Describe the morphology of the erythrocytes.
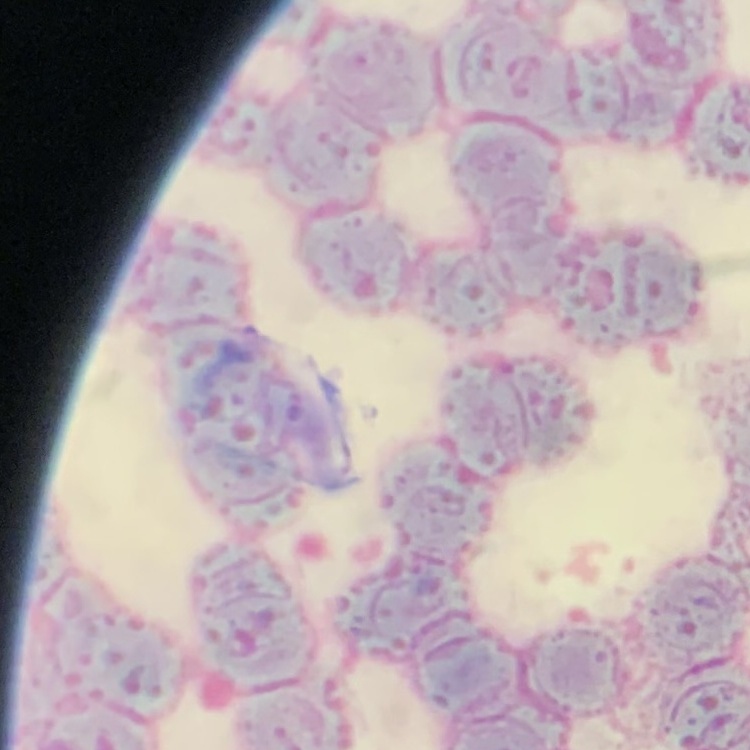

Rouleaux formation.

image type = one tile cut from a larger photomicrograph
stain = Field's or Giemsa
preparation = thin peripheral smear